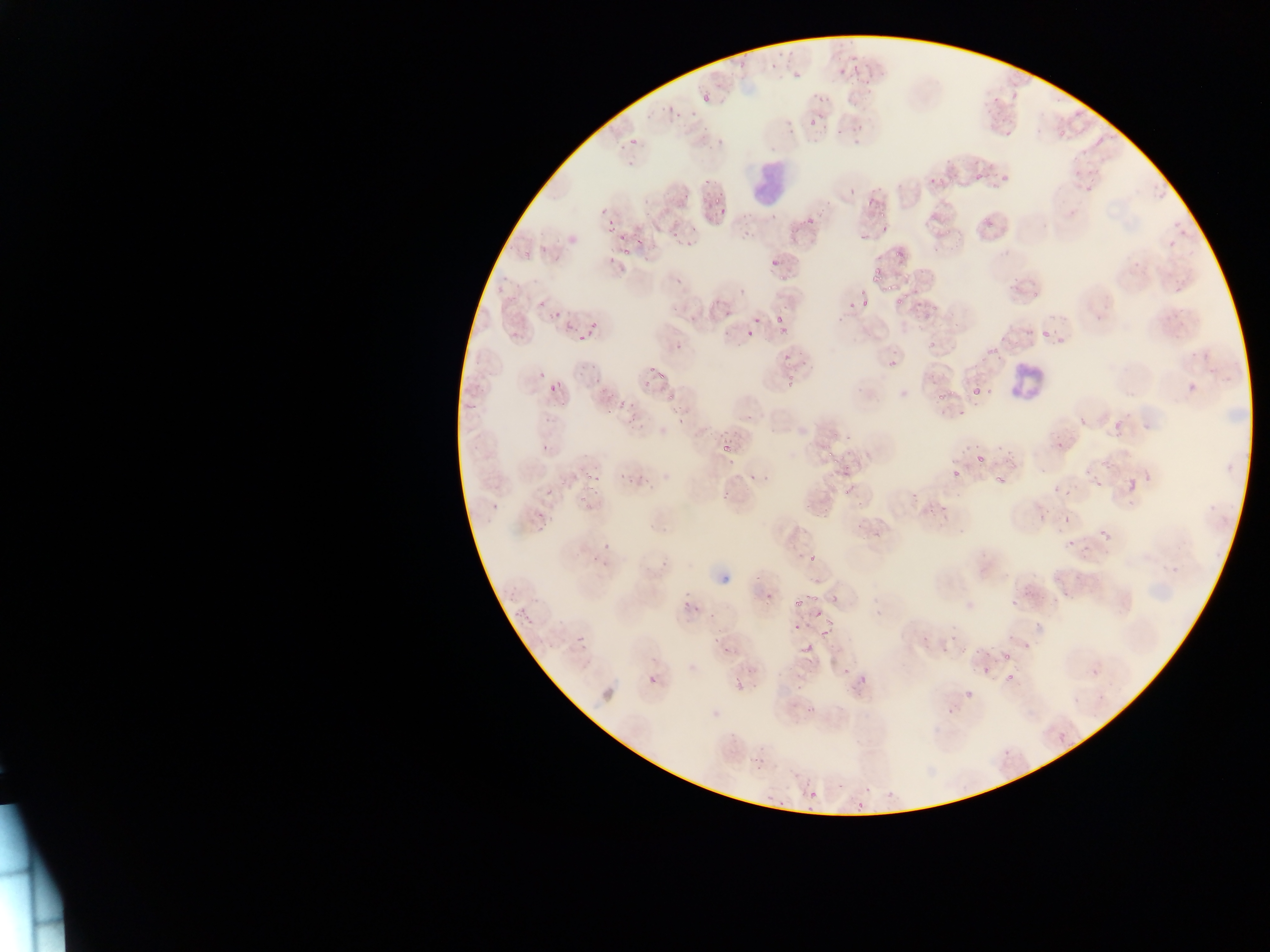
Approximate bounding boxes as left top right bottom in pixels. Leukocyte locations: 749 152 795 206; 1009 361 1055 396. Malaria parasite locations: 767 61 781 69; 851 65 860 71; 793 71 807 81; 699 91 715 101; 666 104 677 118; 807 118 821 128; 630 136 638 149; 975 170 987 180; 703 175 711 186; 1001 175 1009 182; 713 194 726 218; 865 198 876 208; 876 212 887 218; 804 214 814 225; 607 216 620 235; 880 223 894 234; 622 240 633 258; 636 240 649 245; 895 246 903 260; 770 259 781 269; 873 267 881 274; 872 274 879 282; 880 282 894 293; 896 296 907 307; 861 297 873 308; 775 313 785 326; 565 316 576 331; 752 317 761 324; 578 321 600 343; 746 328 752 339; 1041 331 1049 337; 888 358 898 371; 650 364 666 380; 688 374 704 392; 549 377 561 393; 971 387 983 396; 933 392 943 400; 663 396 676 402; 1076 414 1087 425; 1115 421 1122 432; 723 442 731 453; 828 448 844 463; 1004 448 1013 456; 973 454 985 464; 951 467 960 475; 1093 473 1104 488; 994 475 1004 485; 1126 476 1135 493; 843 480 856 500; 1065 488 1073 499; 545 490 555 500; 910 491 920 499; 940 505 952 512; 1062 514 1070 523; 1095 524 1112 540; 810 553 819 561; 810 591 819 605; 829 593 838 606; 796 599 807 606; 681 601 694 610; 811 604 823 618; 515 606 527 620; 524 615 533 626; 793 621 805 632; 820 625 833 638; 576 632 588 645; 799 643 818 654; 1002 652 1013 665; 647 673 656 686; 860 674 866 686; 1005 674 1014 682; 731 676 744 690; 966 685 977 699; 808 786 818 800; 856 799 863 810 | approximate x y pixel centers of objects too small to bound: 588 476. One field of view. Collected in Ghana. Thin blood smear. Mobile-phone photograph taken through the microscope. Image is 1270×952 pixels.